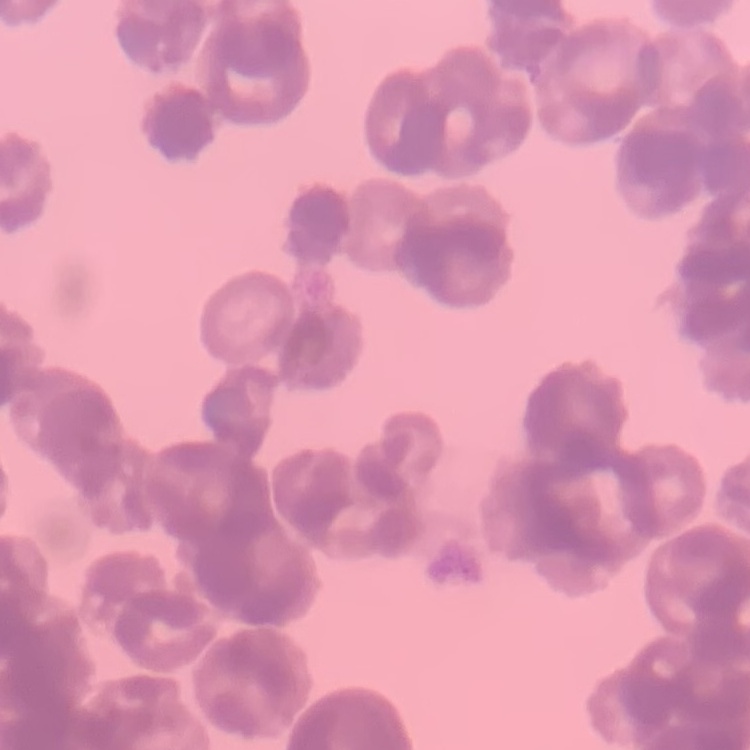

erythrocyte morphology = rouleaux formation
image type = square crop of a larger photomicrograph
preparation = thin blood smear
stain = Field's or Giemsa